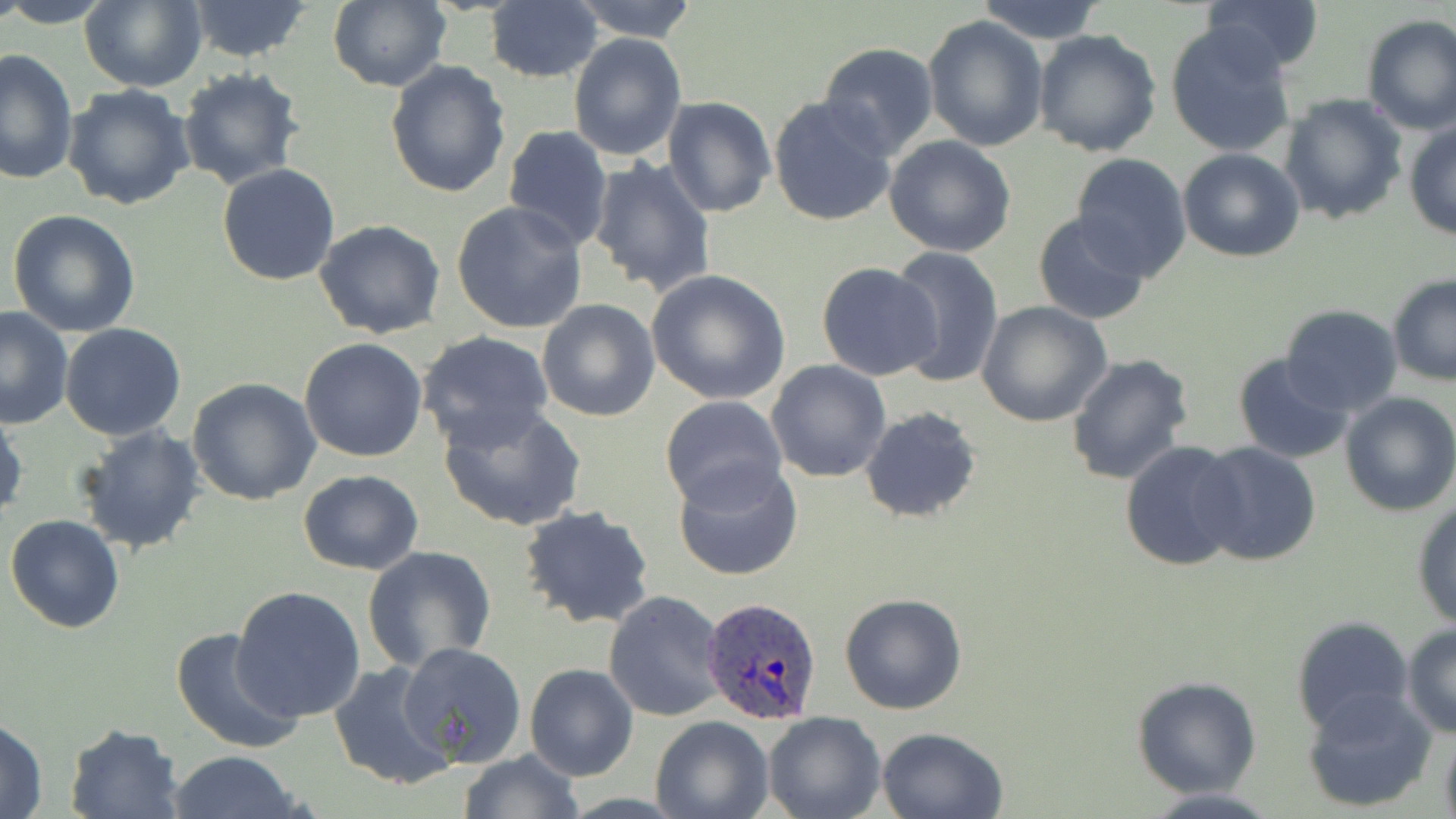

Approximate bounding boxes as (x1, y1, x2, y2) in pixels. Uninfected red blood cell locations: (0, 0, 113, 27), (78, 0, 205, 92), (185, 0, 315, 62), (568, 0, 699, 42), (974, 0, 1107, 43), (1198, 0, 1324, 77), (327, 1, 451, 92), (482, 1, 602, 84), (1359, 13, 1456, 133), (923, 16, 1050, 153), (1165, 24, 1296, 158), (1033, 29, 1163, 157), (568, 32, 687, 160), (816, 43, 939, 160), (1, 47, 78, 186), (384, 59, 511, 198), (178, 67, 305, 190), (63, 82, 195, 210), (1277, 92, 1408, 227), (662, 96, 778, 219), (767, 96, 898, 228), (1403, 118, 1456, 240), (502, 124, 614, 252), (883, 135, 1018, 258), (1178, 148, 1305, 262), (1070, 154, 1194, 280), (585, 156, 717, 298), (217, 164, 340, 286), (450, 201, 589, 335), (7, 210, 141, 337), (1032, 213, 1152, 326), (315, 219, 446, 338), (885, 247, 1005, 387), (815, 264, 943, 381), (644, 269, 793, 406), (1387, 274, 1456, 386), (537, 299, 659, 423), (975, 301, 1114, 427), (0, 305, 75, 430), (1279, 305, 1403, 415), (60, 323, 186, 440), (417, 330, 554, 449), (299, 338, 428, 462), (1065, 352, 1194, 487), (1231, 352, 1354, 464), (766, 360, 890, 482), (187, 378, 321, 505), (1338, 391, 1456, 516), (659, 395, 788, 512), (437, 402, 587, 531), (859, 407, 983, 523), (0, 409, 26, 524), (75, 425, 206, 554), (1119, 440, 1247, 574), (1194, 441, 1322, 567), (672, 456, 804, 583), (297, 469, 425, 575), (1411, 497, 1456, 630), (518, 503, 658, 630), (5, 514, 126, 634), (362, 545, 496, 671), (232, 586, 367, 724), (603, 590, 727, 722), (838, 592, 967, 714), (1291, 615, 1415, 738), (1402, 624, 1456, 738), (172, 626, 302, 753), (398, 641, 527, 767), (329, 661, 459, 791), (525, 664, 638, 782), (1130, 675, 1263, 799), (1302, 689, 1436, 813), (763, 712, 885, 819), (0, 715, 49, 819), (649, 716, 773, 819), (64, 723, 185, 819), (1437, 724, 1456, 819), (876, 726, 1009, 819), (455, 749, 585, 819), (169, 751, 305, 819), (1137, 788, 1287, 819). Plasmodium ovale-infected red blood cell locations: (702, 596, 824, 724). Slide-level diagnosis: Plasmodium ovale. Optical microscopy. Image is 1456×819 pixels. Captured at 1000x magnification. One field of a larger specimen. Thin blood smear. May-Grünwald-Giemsa stain.